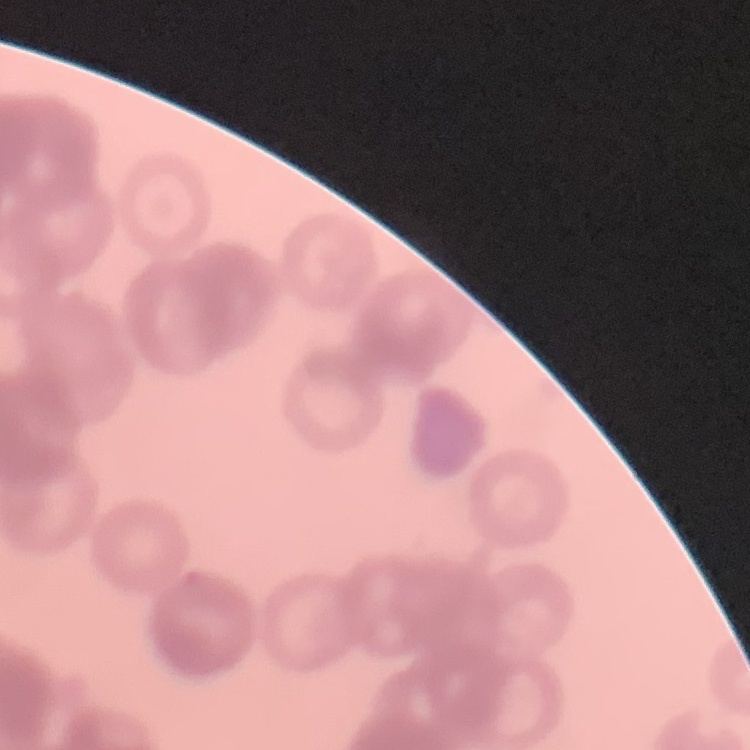
Summary:
  - Red blood cell morphology: rouleaux formation
  - Stain: Field's or Giemsa
  - Image type: square crop of a larger photomicrograph
  - Preparation: thin peripheral smear